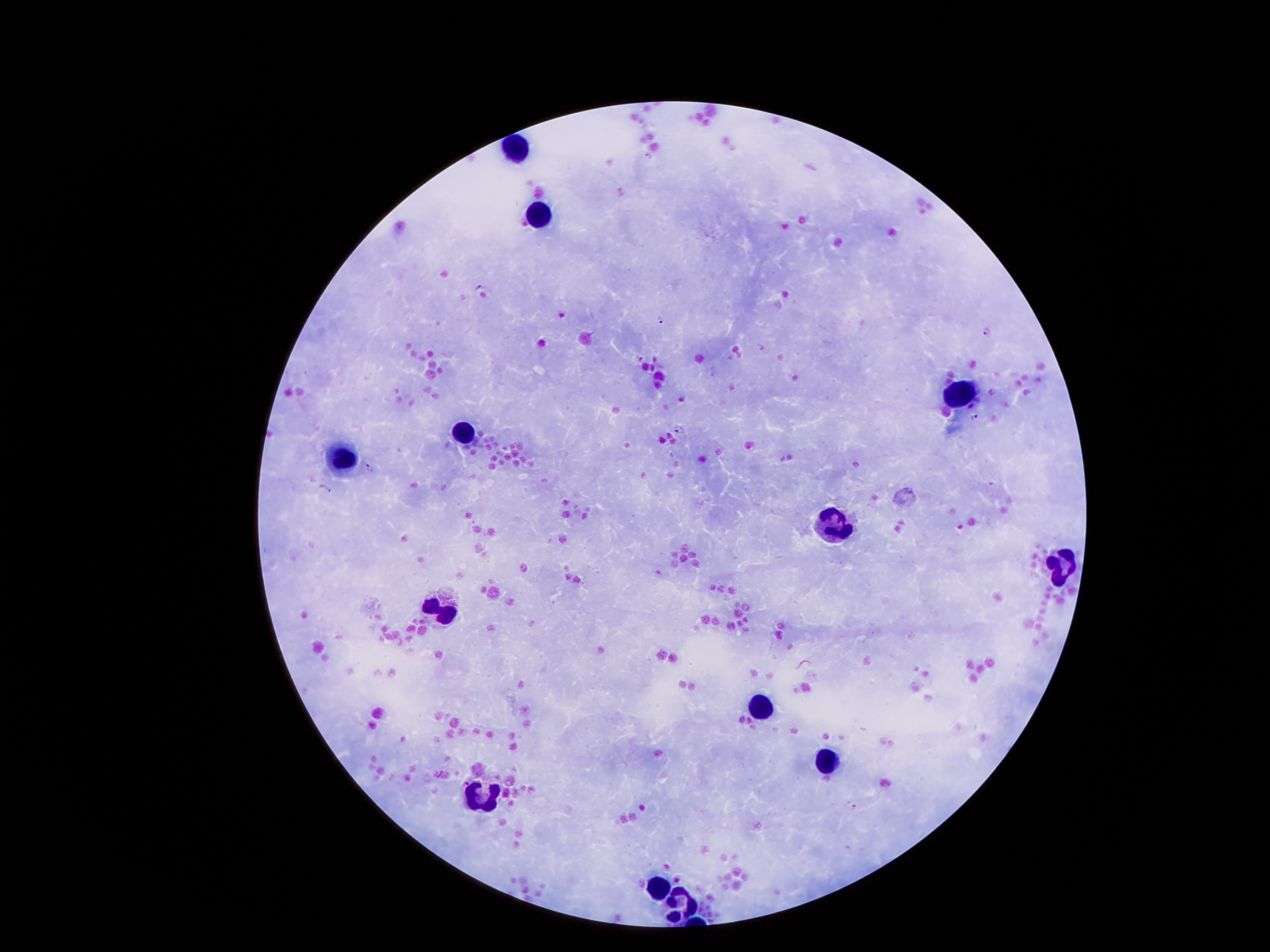

coordinate format = approximate centers as [x, y] in pixels
Plasmodium parasite locations = [648, 155], [480, 288], [662, 320], [986, 330], [976, 418], [678, 430], [369, 468], [325, 488], [854, 807]
leukocyte locations = [517, 145], [542, 213], [958, 393], [463, 434], [338, 454], [835, 530], [1062, 568], [447, 611], [758, 708], [824, 763], [485, 797], [658, 888], [687, 904]
image size = 1270×952 pixels
magnification = 100x
field of view = one from this slide
preparation = thick blood smear
stain = Giemsa
capture = smartphone through the microscope eyepiece
patient malaria status = infected with Plasmodium falciparum